Comment on the morphology of the erythrocytes.
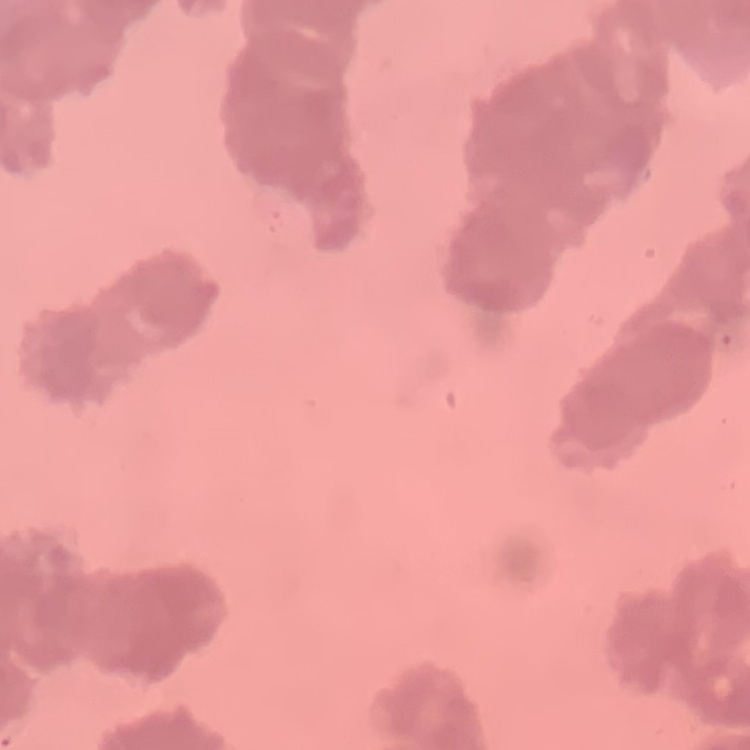
Rouleaux formation.

image type = one tile cut from a larger photomicrograph
preparation = thin peripheral smear
stain = Field's or Giemsa